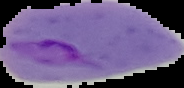

Image is 184×88 pixels. Result: malaria parasites identified. The area outside the segmented cell region is set to black. From a thin blood film.